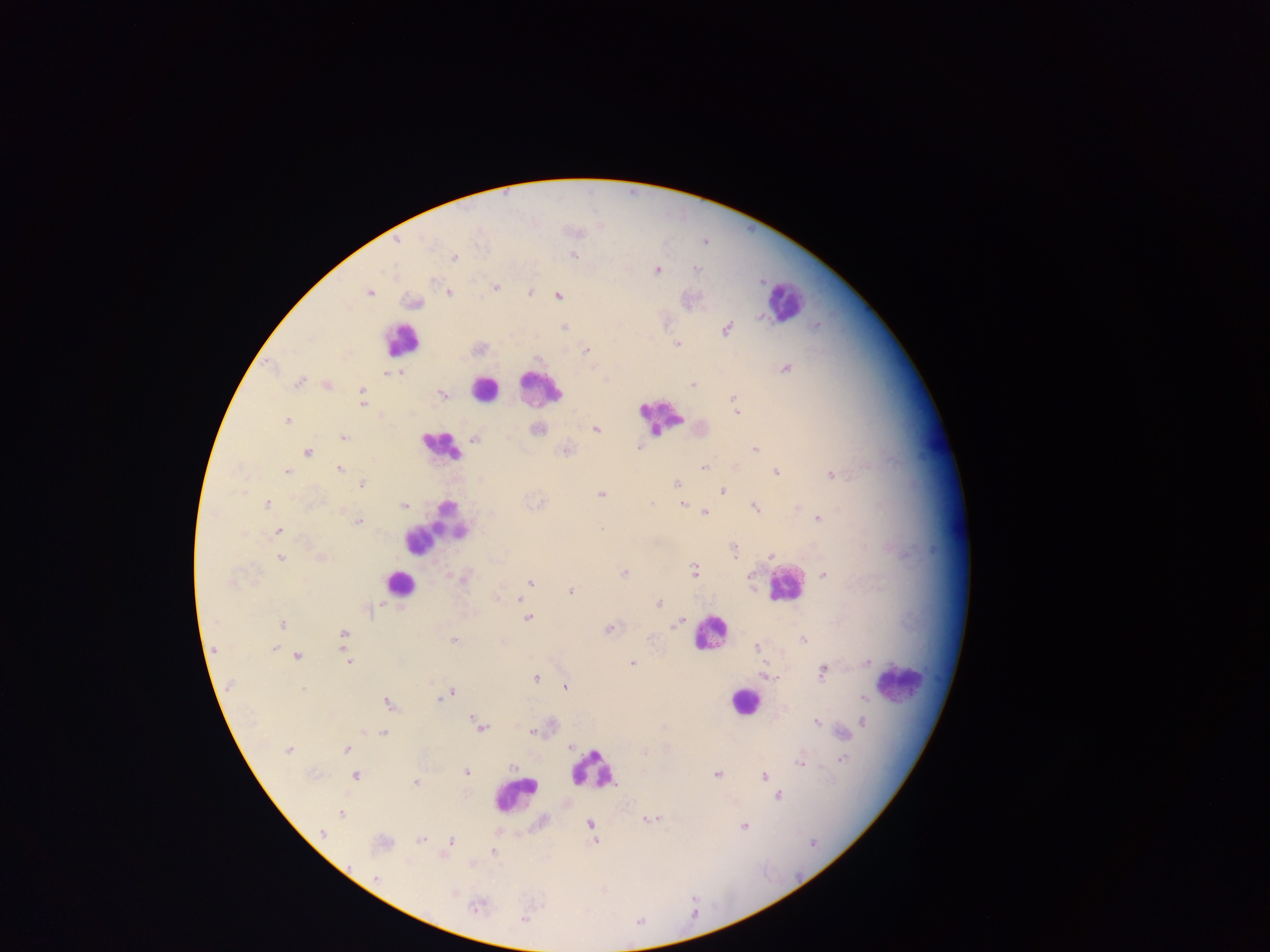
Approximate centers as (x, y) in pixels. Leukocyte locations (subset; some below the resolvable size): (785, 302), (400, 340), (540, 388), (484, 389), (662, 416), (439, 446), (436, 527), (400, 583), (783, 584), (710, 633), (905, 682), (744, 701), (593, 769), (514, 794). Malaria parasite locations: (398, 241), (573, 255), (454, 257), (697, 269), (656, 270), (495, 287), (449, 292), (530, 292), (369, 293), (558, 295), (415, 303), (564, 327), (726, 329), (677, 344), (587, 351), (786, 368), (398, 371), (384, 373), (300, 383), (693, 384), (327, 386), (362, 389), (442, 395), (362, 396), (733, 398), (362, 405), (735, 412), (286, 421), (596, 429), (538, 430), (343, 437), (474, 438), (638, 447), (755, 449), (307, 452), (703, 467), (340, 468), (775, 471), (287, 472), (831, 474), (677, 483), (362, 484), (722, 491), (601, 494), (267, 504), (653, 504), (682, 504), (404, 506), (755, 508), (705, 512), (818, 518), (358, 522), (279, 531), (734, 551), (770, 556), (322, 557), (280, 558), (694, 570), (624, 573), (823, 575), (464, 578), (530, 582), (231, 584), (570, 590), (496, 599), (520, 600), (659, 603), (374, 609), (527, 617), (678, 623), (283, 624), (608, 628), (343, 634), (803, 639), (454, 641), (757, 648), (274, 649), (297, 655), (348, 662), (633, 663), (822, 672), (767, 675), (535, 677), (230, 685), (565, 687), (303, 689), (451, 693), (446, 696), (864, 698), (440, 699), (388, 703), (817, 722), (863, 722), (480, 726), (532, 731), (383, 734), (571, 746), (346, 748), (288, 750), (644, 752), (841, 759), (799, 763), (466, 772), (717, 774), (355, 776), (764, 776), (415, 783), (778, 796), (341, 814), (649, 819), (589, 825), (745, 826), (322, 834), (421, 839), (451, 841), (594, 841), (493, 850), (377, 878), (476, 907), (523, 919). Mobile-phone photograph taken through the microscope. Sample from Ghana. One field of view. Thick blood film. Image is 1270×952 pixels.